Give the preparation type.
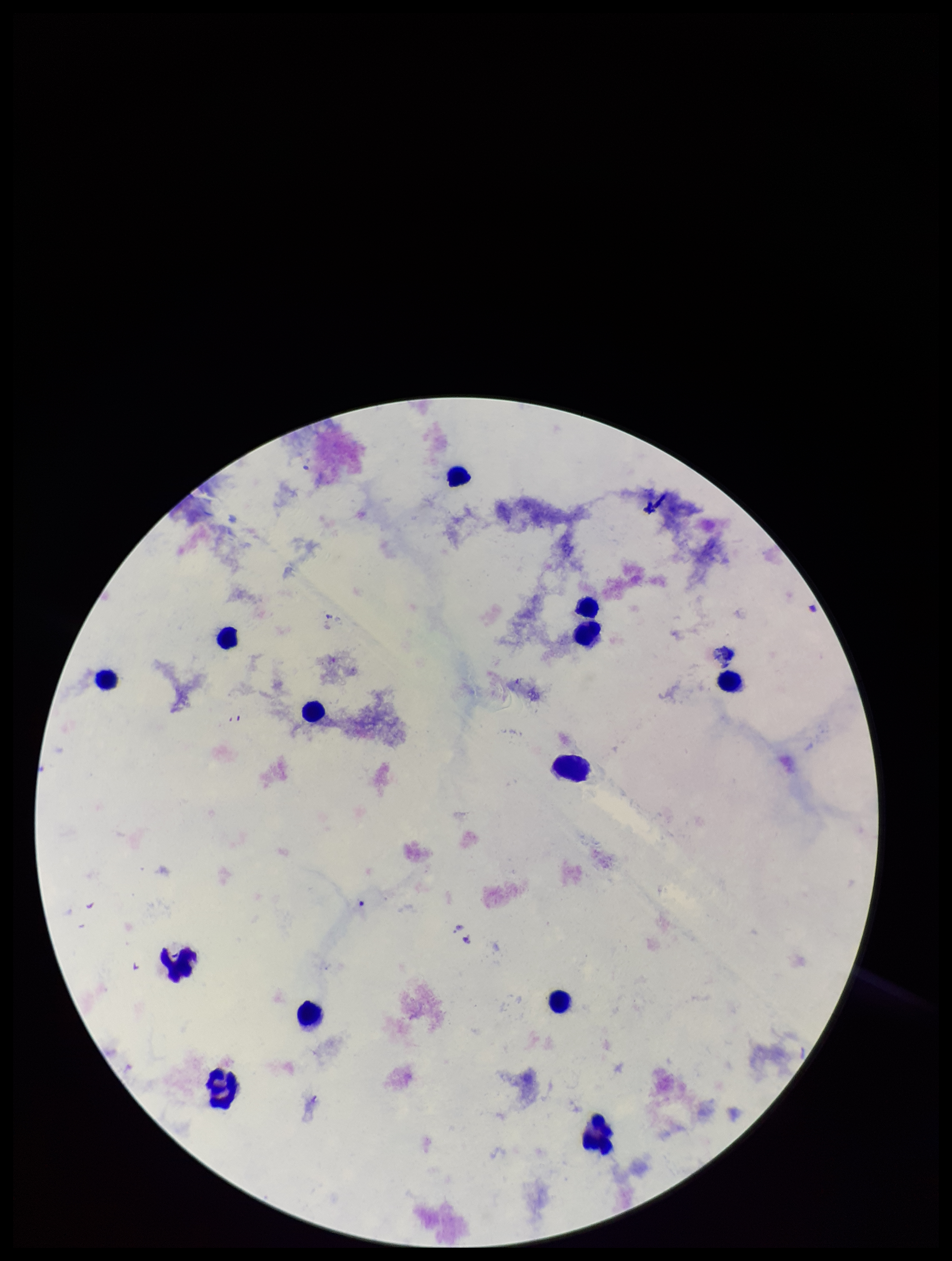
It is a thick blood smear.

Summary:
  - Patient malaria status: negative
  - Leukocyte count: 13
  - Capture: smartphone photograph through the microscope eyepiece
  - Plasmodium parasites: none seen
  - Field of view: single
  - Parasite count: 0
  - Image size: 952×1261 pixels
  - Stain: Giemsa